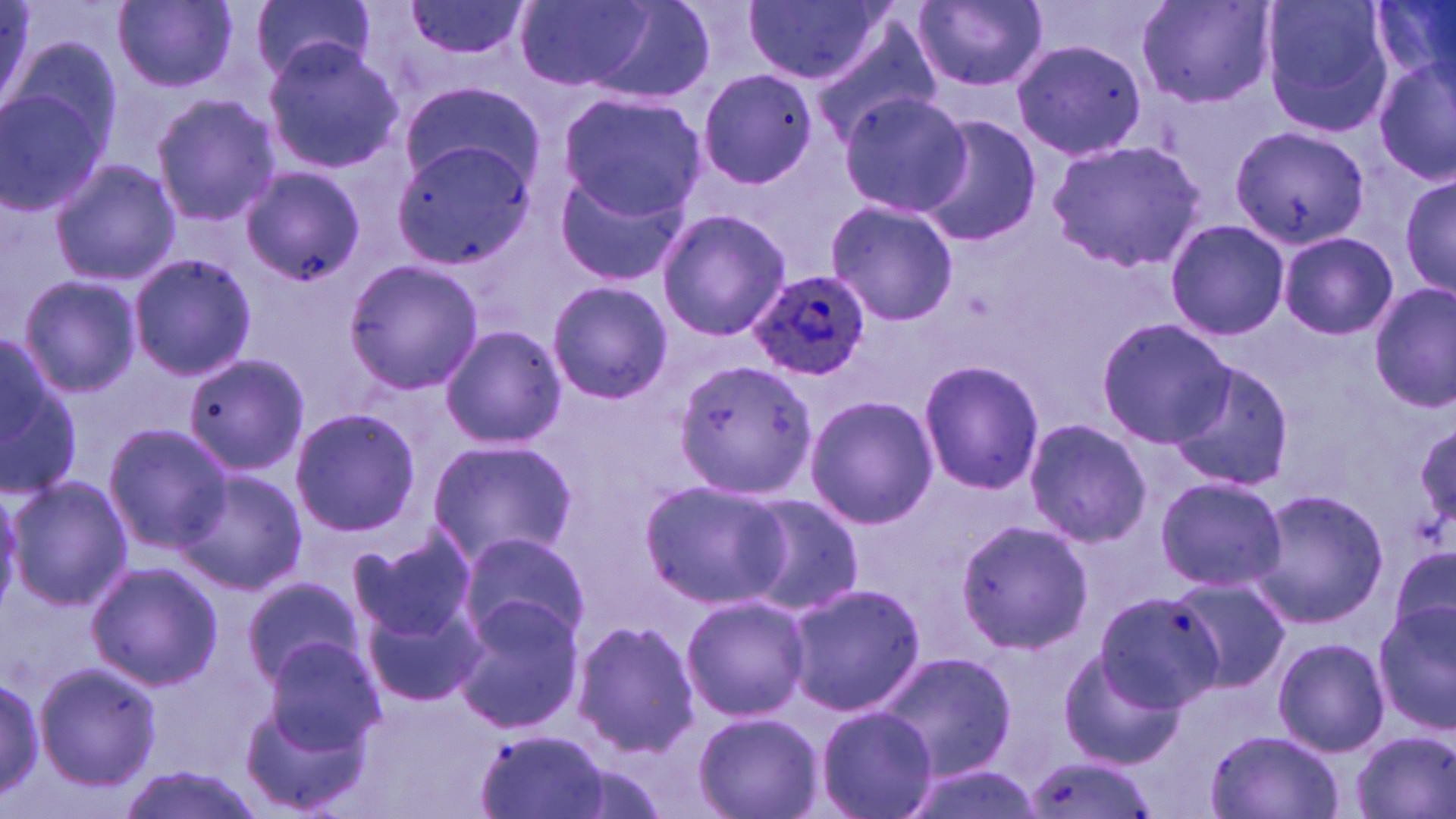
Approximate bounding boxes as named x1/y1/x2/y2 corners in pixels. Plasmodium ovale-infected red blood cell locations: (x1=749, y1=267, x2=871, y2=382). Uninfected red blood cell locations: (x1=114, y1=0, x2=237, y2=92), (x1=402, y1=0, x2=531, y2=62), (x1=744, y1=0, x2=891, y2=85), (x1=912, y1=0, x2=1048, y2=94), (x1=1133, y1=0, x2=1278, y2=111), (x1=1260, y1=0, x2=1396, y2=137), (x1=1369, y1=0, x2=1456, y2=95), (x1=248, y1=1, x2=375, y2=81), (x1=510, y1=1, x2=691, y2=98), (x1=811, y1=26, x2=943, y2=144), (x1=7, y1=33, x2=122, y2=165), (x1=1008, y1=35, x2=1147, y2=162), (x1=261, y1=38, x2=405, y2=174), (x1=1373, y1=55, x2=1456, y2=188), (x1=697, y1=70, x2=816, y2=189), (x1=400, y1=79, x2=545, y2=194), (x1=0, y1=88, x2=109, y2=213), (x1=555, y1=91, x2=706, y2=220), (x1=836, y1=92, x2=970, y2=217), (x1=150, y1=94, x2=282, y2=228), (x1=914, y1=117, x2=1042, y2=247), (x1=1228, y1=123, x2=1369, y2=249), (x1=392, y1=126, x2=540, y2=267), (x1=1047, y1=139, x2=1207, y2=273), (x1=49, y1=160, x2=182, y2=286), (x1=552, y1=165, x2=694, y2=291), (x1=238, y1=166, x2=365, y2=286), (x1=1398, y1=172, x2=1455, y2=302), (x1=825, y1=201, x2=959, y2=326), (x1=655, y1=208, x2=790, y2=341), (x1=1165, y1=218, x2=1288, y2=340), (x1=1278, y1=231, x2=1397, y2=340), (x1=129, y1=253, x2=258, y2=381), (x1=342, y1=260, x2=484, y2=395), (x1=16, y1=275, x2=143, y2=399), (x1=545, y1=279, x2=673, y2=406), (x1=1369, y1=283, x2=1455, y2=414), (x1=1099, y1=318, x2=1235, y2=446), (x1=438, y1=323, x2=567, y2=451), (x1=0, y1=341, x2=82, y2=494), (x1=181, y1=351, x2=309, y2=478), (x1=917, y1=357, x2=1045, y2=496), (x1=675, y1=360, x2=816, y2=501), (x1=1166, y1=360, x2=1293, y2=492), (x1=805, y1=393, x2=938, y2=529), (x1=288, y1=406, x2=420, y2=537), (x1=1021, y1=418, x2=1150, y2=545), (x1=1414, y1=420, x2=1456, y2=537), (x1=103, y1=422, x2=233, y2=555), (x1=425, y1=439, x2=576, y2=568), (x1=177, y1=466, x2=306, y2=596), (x1=7, y1=474, x2=134, y2=608), (x1=1154, y1=475, x2=1285, y2=594), (x1=639, y1=477, x2=788, y2=608), (x1=1248, y1=486, x2=1389, y2=628), (x1=742, y1=491, x2=866, y2=616), (x1=955, y1=518, x2=1096, y2=654), (x1=348, y1=530, x2=478, y2=643), (x1=453, y1=533, x2=590, y2=651), (x1=1391, y1=542, x2=1456, y2=646), (x1=85, y1=562, x2=224, y2=690), (x1=242, y1=576, x2=365, y2=691), (x1=1165, y1=576, x2=1288, y2=694), (x1=786, y1=581, x2=925, y2=717), (x1=1088, y1=593, x2=1221, y2=713), (x1=679, y1=595, x2=811, y2=723), (x1=362, y1=597, x2=485, y2=709), (x1=451, y1=598, x2=585, y2=735), (x1=1374, y1=602, x2=1456, y2=736), (x1=570, y1=619, x2=701, y2=759), (x1=1271, y1=637, x2=1391, y2=757), (x1=261, y1=638, x2=387, y2=754), (x1=1056, y1=648, x2=1184, y2=770), (x1=875, y1=649, x2=1018, y2=781), (x1=34, y1=661, x2=162, y2=790), (x1=241, y1=668, x2=382, y2=815), (x1=0, y1=669, x2=55, y2=797), (x1=816, y1=705, x2=937, y2=819), (x1=693, y1=711, x2=823, y2=819), (x1=471, y1=729, x2=613, y2=819), (x1=1206, y1=731, x2=1344, y2=819), (x1=1350, y1=731, x2=1455, y2=818), (x1=1018, y1=757, x2=1157, y2=819), (x1=118, y1=765, x2=264, y2=819), (x1=900, y1=765, x2=1045, y2=819). Slide-level diagnosis: Plasmodium ovale. May-Grünwald-Giemsa-stained preparation. Thin blood smear. Single field of view. Light microscopy. Image is 1456×819 pixels. 1000x magnification.